Report the malaria status of this cell.
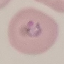
Parasitized.

Summary:
  - Stain: Giemsa
  - Preparation: thin smear
  - Capture: smartphone through the microscope eyepiece
  - Image type: cell patch, automatically extracted from a larger field of view and resized to 64 × 64 pixels